Give the position of every P. falciparum parasite, noting its life-cycle stage.
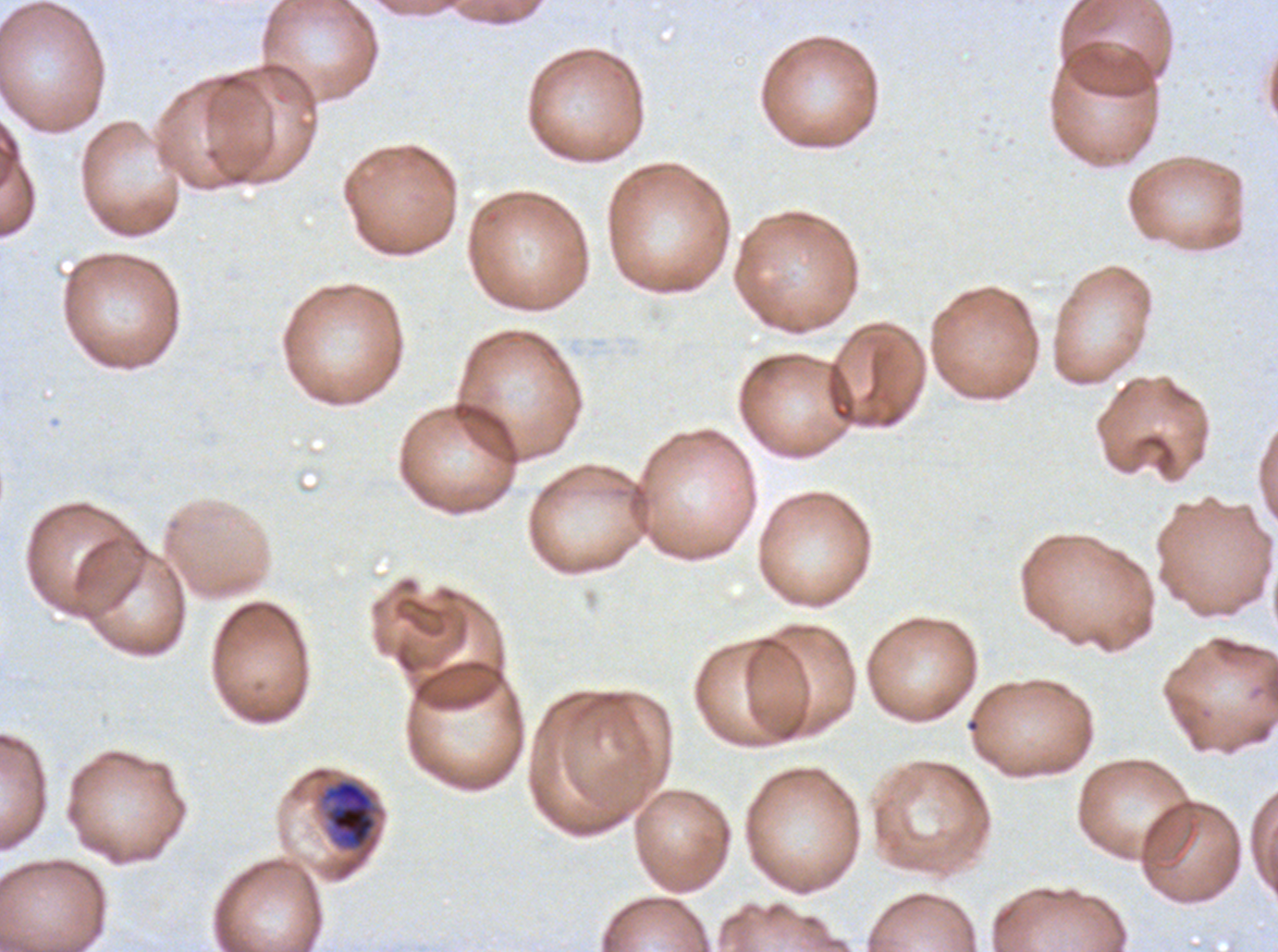

Approximate bounding boxes as [x1, y1, x2, y2] in pixels.
Late trophozoites: [322, 778, 377, 850].
No rings, late-ring/early-trophozoite forms, mid trophozoites, early schizonts, late schizonts, segmenters, or gametocytes observed.

Ex-vivo P. falciparum culture from a patient in The Gambia, grown for 24 to 48 hours. Thin blood smear. Image is 1278×952 pixels. One sub-image of a larger composite. Giemsa stain.